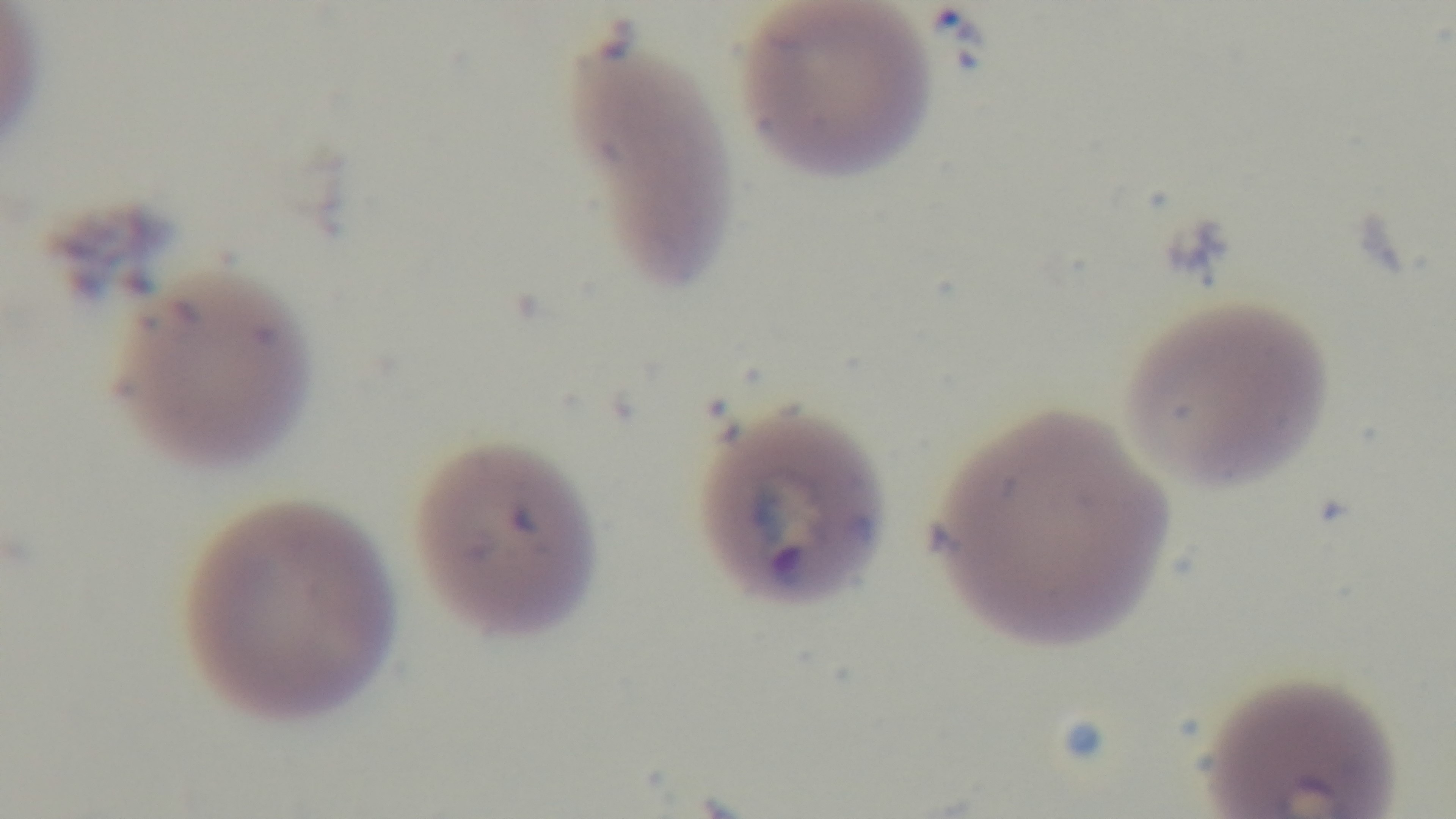
Preparation: thin smear. Captured with a mounted 4K digital camera. Giemsa-stained. Single field of view. 100x oil-immersion objective. Malaria status: positive. Photomicrograph.